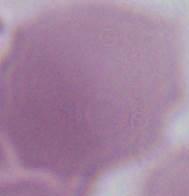
Summary:
  - Identification: red blood cell
  - Magnification: 1000x
  - Modality: photomicrograph